Classify this cell by malaria status.
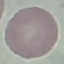
Uninfected.

Thin smear of blood. Cell patch, automatically extracted from a larger field of view and resized to 64 × 64 pixels. Acquired by smartphone through the microscope eyepiece. Giemsa stain.